Identify the blood parasite species.
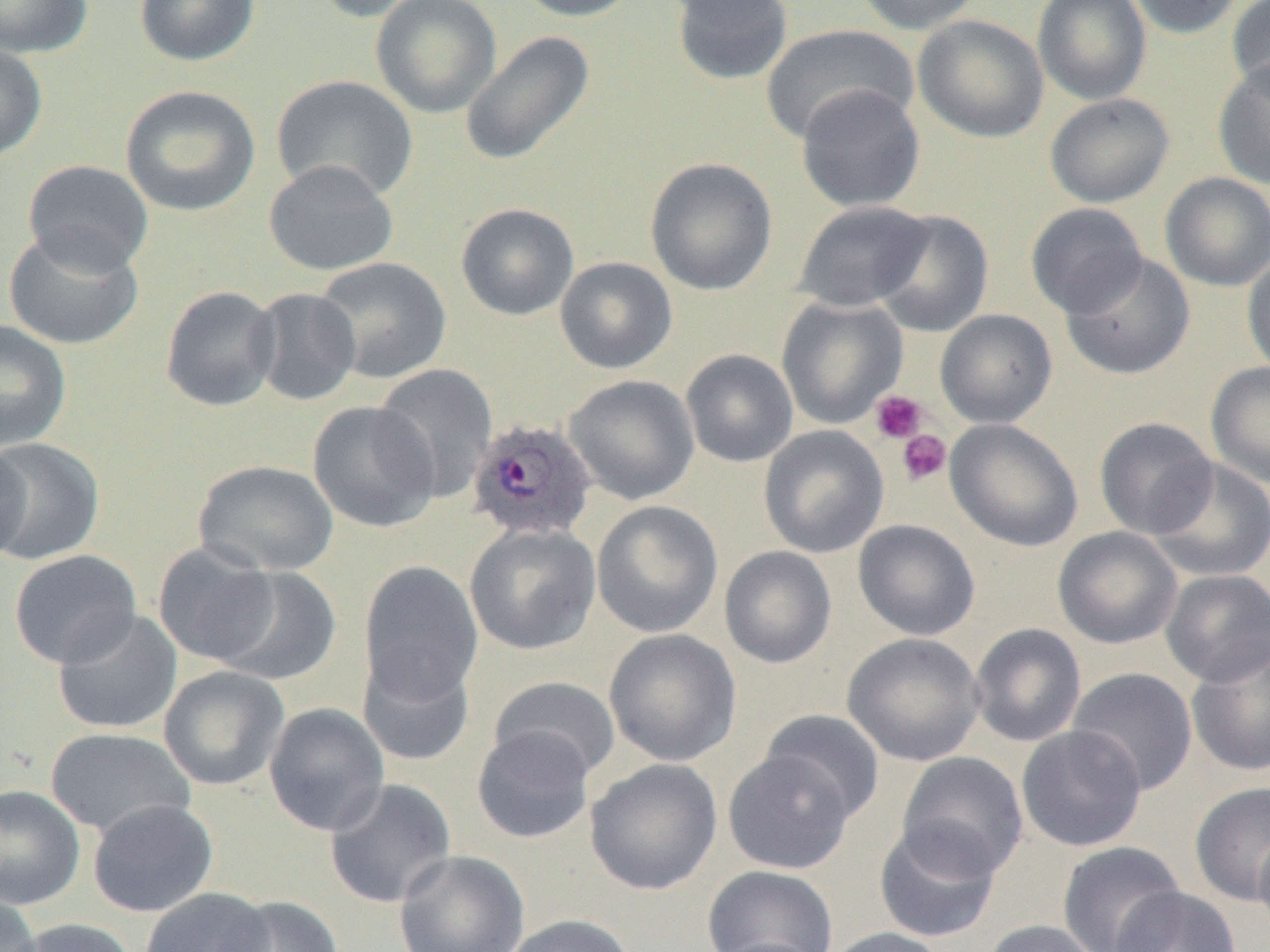
Plasmodium ovale.

Approximate bounding boxes as [x1, y1, x2, y2] in pixels. Platelet locations: [869, 390, 928, 444], [897, 429, 951, 486]. Plasmodium ovale-infected red blood cell locations: [465, 417, 598, 543]. Uninfected red blood cell locations: [0, 0, 93, 57], [134, 0, 260, 66], [312, 0, 435, 23], [370, 0, 502, 119], [511, 0, 647, 22], [670, 0, 793, 86], [851, 0, 983, 35], [1032, 0, 1152, 105], [1125, 0, 1248, 39], [1227, 0, 1270, 100], [912, 14, 1050, 144], [760, 24, 918, 145], [459, 30, 596, 167], [0, 42, 48, 163], [1213, 58, 1270, 190], [271, 75, 419, 203], [795, 84, 926, 213], [120, 85, 261, 217], [1044, 93, 1174, 208], [644, 157, 778, 296], [22, 159, 154, 275], [263, 160, 399, 276], [1159, 172, 1270, 291], [793, 200, 934, 312], [456, 203, 579, 321], [1026, 203, 1147, 319], [871, 209, 995, 337], [2, 228, 144, 351], [1060, 251, 1196, 380], [1242, 253, 1270, 380], [314, 256, 452, 383], [554, 256, 678, 374], [160, 285, 282, 411], [249, 287, 362, 406], [776, 296, 909, 429], [935, 309, 1057, 429], [0, 319, 72, 451], [680, 348, 798, 468], [1205, 361, 1270, 488], [373, 363, 498, 503], [563, 374, 700, 506], [307, 400, 440, 532], [1093, 417, 1217, 539], [945, 418, 1084, 552], [758, 425, 889, 558], [0, 436, 105, 565], [0, 437, 31, 568], [1146, 458, 1270, 582], [193, 460, 339, 576], [591, 500, 723, 638], [853, 519, 981, 641], [464, 522, 601, 655], [1052, 526, 1183, 650], [153, 542, 280, 666], [719, 546, 837, 669], [8, 550, 142, 668], [359, 560, 483, 704], [212, 567, 342, 686], [1160, 569, 1270, 687], [52, 608, 183, 735], [969, 623, 1087, 747], [604, 628, 742, 767], [842, 632, 985, 766], [1186, 636, 1270, 778], [357, 648, 476, 767], [159, 665, 290, 791], [1067, 667, 1198, 795], [488, 676, 621, 783], [263, 702, 390, 836], [759, 709, 885, 823], [1016, 725, 1147, 852], [472, 726, 596, 844], [45, 727, 196, 838], [722, 748, 857, 875], [896, 751, 1029, 880], [584, 758, 723, 895], [324, 777, 458, 908], [1190, 781, 1270, 907], [0, 784, 86, 910], [87, 798, 219, 917], [873, 822, 1002, 943], [1254, 831, 1270, 938], [1057, 841, 1185, 952], [394, 849, 530, 952], [702, 864, 839, 952], [1112, 886, 1241, 952], [140, 887, 274, 952], [0, 893, 43, 952], [215, 895, 344, 952], [500, 914, 638, 952], [14, 918, 139, 952], [981, 919, 1106, 952], [822, 927, 951, 952], [706, 937, 831, 952]. Captured at 1000x magnification. Thin blood film. Single field of view. Optical microscopy. Image is 1270×952 pixels.